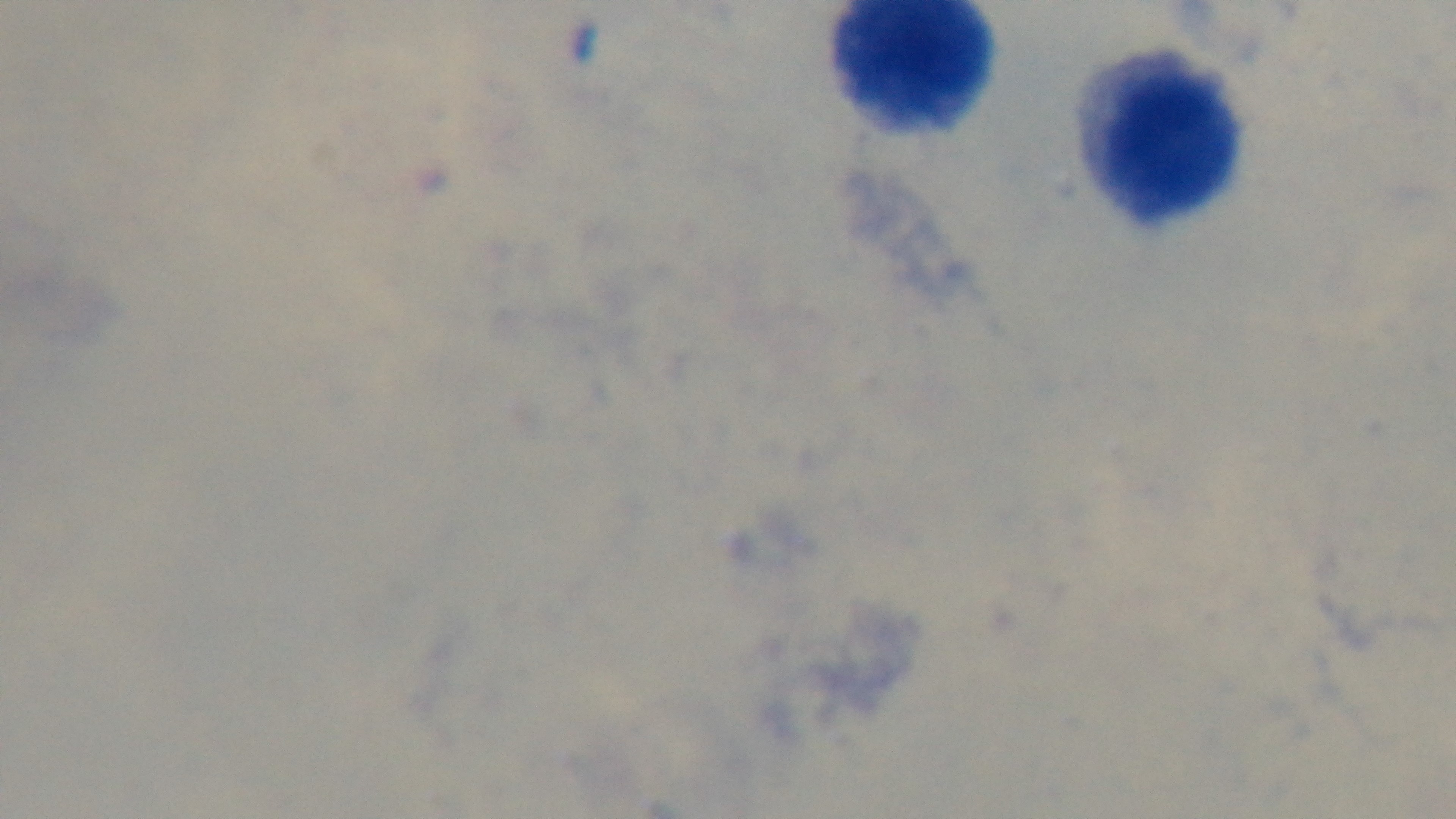

{
  "objective": "100x oil immersion",
  "modality": "light microscopy",
  "stain": "Giemsa",
  "capture": "mounted 4K digital camera",
  "malaria_status": "uninfected",
  "preparation": "thick",
  "field_of_view": "single"
}